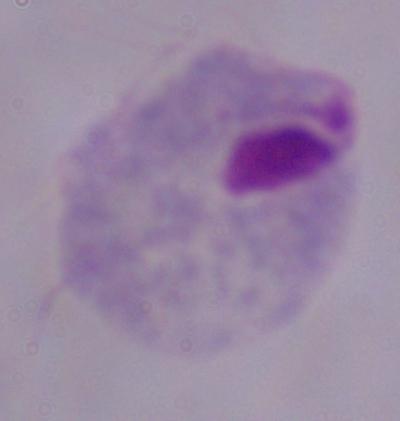

magnification = 1000x
modality = photomicrograph
identification = trichomonad